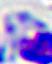

400x magnification. Photomicrograph. A leukocyte is seen.